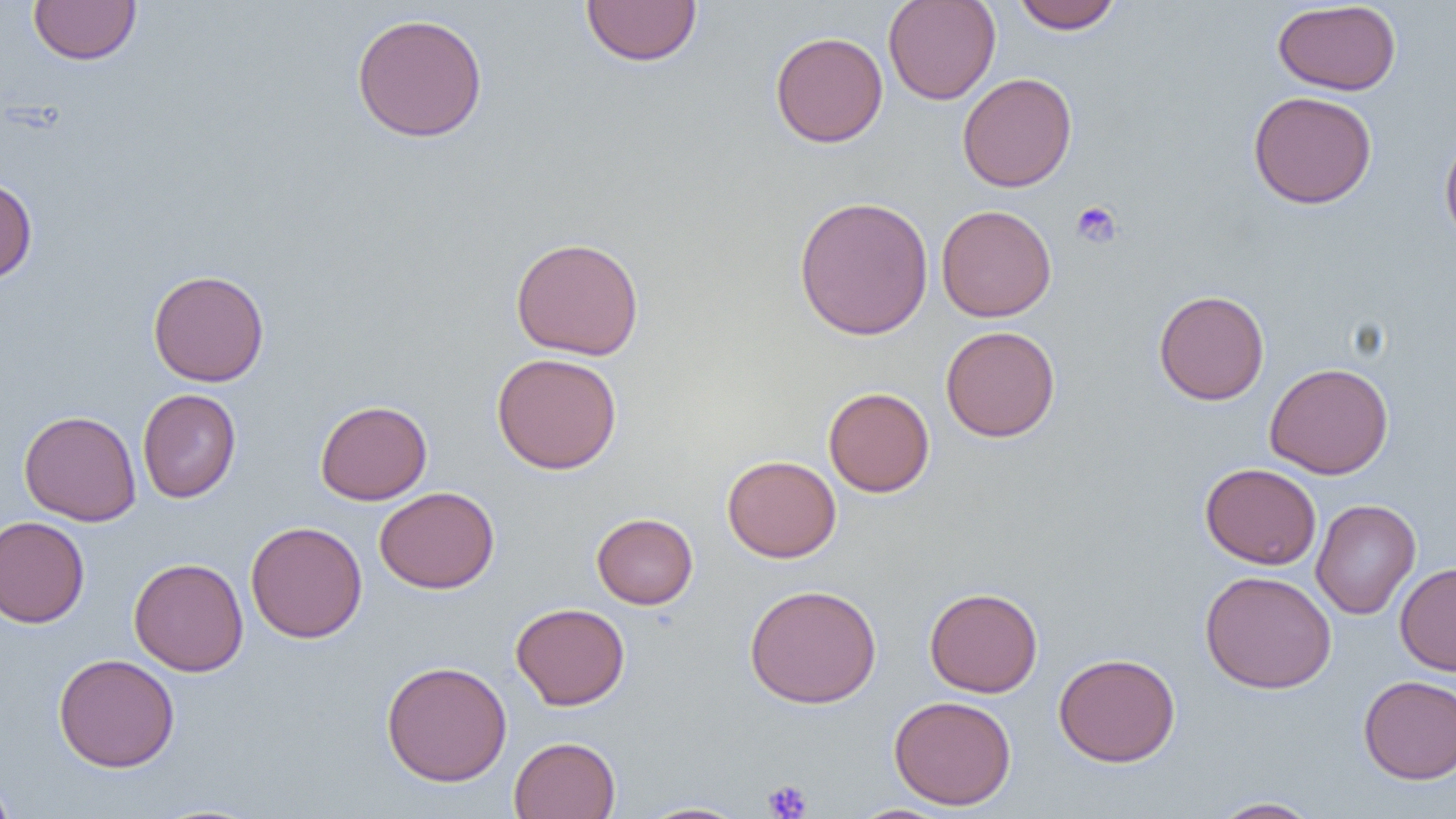
Summary:
  - Coordinate format: approximate bounding boxes as (x1,y1)-(x2,y2) corner pairs in pixels
  - Platelet locations: (1071,201)-(1122,249), (763,780)-(813,819)
  - Uninfected red blood cell locations: (28,0)-(142,65), (581,0)-(702,66), (883,0)-(1001,105), (1011,0)-(1123,34), (1272,1)-(1401,95), (351,12)-(488,143), (770,31)-(888,148), (957,73)-(1077,192), (1248,90)-(1377,210), (1439,128)-(1456,250), (0,176)-(37,284), (793,195)-(934,341), (936,204)-(1057,322), (511,236)-(645,361), (148,269)-(269,387), (1153,289)-(1269,405), (940,325)-(1060,442), (492,352)-(623,474), (1265,362)-(1394,479), (823,387)-(935,497), (137,389)-(241,503), (315,400)-(432,505), (18,410)-(142,526), (722,454)-(841,563), (1200,463)-(1321,569), (375,486)-(499,593), (1310,499)-(1421,619), (592,512)-(698,609), (0,516)-(90,628), (245,521)-(367,643), (128,557)-(248,676), (1395,562)-(1456,676), (1200,570)-(1337,694), (744,583)-(882,709), (924,586)-(1043,697), (511,602)-(630,710), (1053,652)-(1181,767), (53,653)-(180,772), (381,660)-(512,786), (1358,675)-(1456,784), (889,695)-(1017,810), (509,736)-(621,819), (0,772)-(16,819), (1209,797)-(1323,818), (635,800)-(751,818), (849,804)-(953,819)
  - Slide-level diagnosis: no evidence of blood parasites
  - Preparation: thin blood film
  - Image size: 1456×819 pixels
  - Magnification: 1000x
  - Modality: optical microscopy
  - Field of view: one of a larger specimen